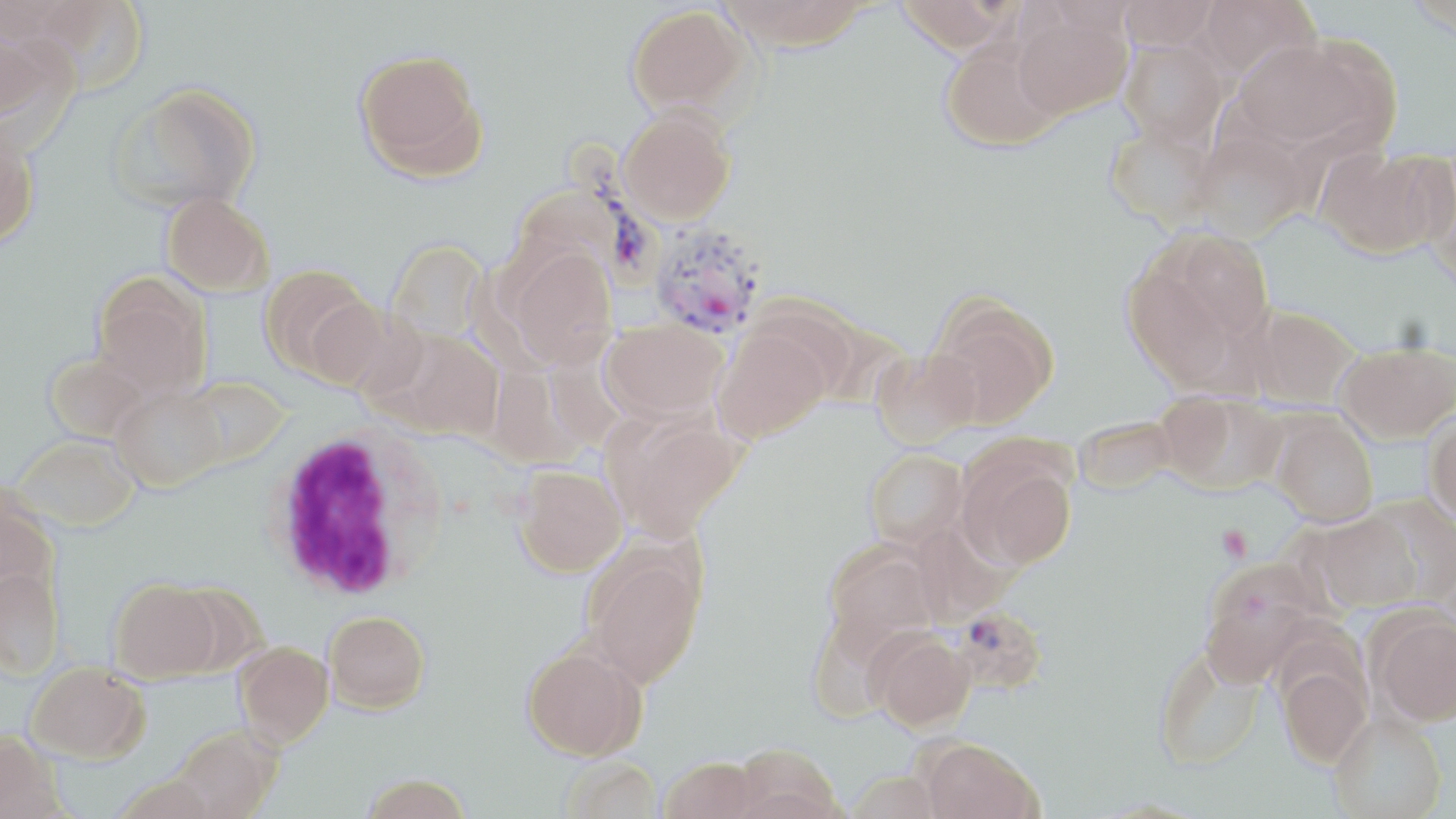

slide_level_diagnosis: Plasmodium vivax
white_blood_cell_locations: 'approximate bounding boxes as [x1, y1, x2, y2] in pixels: [265, 426, 447, 602]'
modality: light microscopy
stain: May-Grünwald-Giemsa
plasmodium_vivax_infected_red_blood_cell_locations: 'approximate bounding boxes as [x1, y1, x2, y2] in pixels: [566, 133, 666, 296], [648, 223, 768, 339], [953, 604, 1047, 695]'
field_of_view: single
platelet_locations: 'approximate bounding boxes as [x1, y1, x2, y2] in pixels: [1216, 524, 1252, 562]'
magnification: 1000x
uninfected_red_blood_cell_locations: 'approximate bounding boxes as [x1, y1, x2, y2] in pixels: [29, 0, 149, 95], [717, 0, 873, 51], [893, 0, 1021, 55], [1118, 0, 1221, 51], [1195, 0, 1321, 85], [626, 5, 749, 115], [1012, 9, 1132, 120], [0, 25, 78, 150], [1232, 37, 1379, 154], [1119, 38, 1230, 149], [940, 39, 1065, 152], [354, 49, 487, 179], [111, 84, 261, 213], [619, 108, 735, 224], [1105, 123, 1218, 227], [0, 128, 39, 248], [1190, 128, 1314, 239], [1316, 147, 1447, 260], [161, 193, 273, 296], [1155, 230, 1276, 350], [387, 240, 489, 344], [506, 247, 618, 369], [1121, 257, 1249, 390], [259, 264, 377, 379], [92, 277, 211, 399], [306, 297, 413, 394], [930, 299, 1058, 428], [1246, 307, 1359, 408], [601, 318, 727, 421], [712, 326, 832, 444], [382, 329, 505, 441], [1337, 342, 1456, 442], [871, 347, 980, 448], [45, 354, 150, 444], [183, 376, 289, 467], [113, 386, 227, 491], [1159, 391, 1285, 495], [604, 411, 744, 538], [1270, 413, 1378, 527], [1426, 414, 1456, 524], [1073, 415, 1179, 495], [13, 435, 140, 532], [956, 444, 1078, 570], [864, 450, 968, 550], [516, 465, 627, 576], [0, 489, 58, 600], [1367, 494, 1456, 604], [1314, 513, 1422, 612], [823, 544, 939, 656], [582, 546, 705, 686], [1199, 560, 1321, 685], [0, 567, 63, 679], [110, 580, 222, 682], [324, 610, 430, 712], [1371, 610, 1456, 726], [869, 630, 975, 731], [235, 642, 334, 746], [522, 645, 646, 760], [1154, 648, 1265, 771], [1278, 662, 1371, 766], [26, 663, 147, 763], [1329, 712, 1446, 819], [174, 726, 281, 819], [0, 730, 60, 818], [921, 737, 1042, 819], [732, 743, 843, 819], [659, 756, 762, 819], [560, 757, 663, 819], [844, 772, 946, 818], [112, 775, 222, 819], [360, 775, 473, 819]'
image_size: 1456×819 pixels
preparation: thin blood smear